Report the malaria status of this cell.
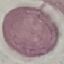

It is uninfected.

Summary:
  - Preparation: thin blood smear
  - Capture: smartphone camera at the microscope eyepiece
  - Image type: cell patch, automatically extracted from a larger field of view and resized to 64 × 64 pixels
  - Stain: Giemsa